State the preparation type.
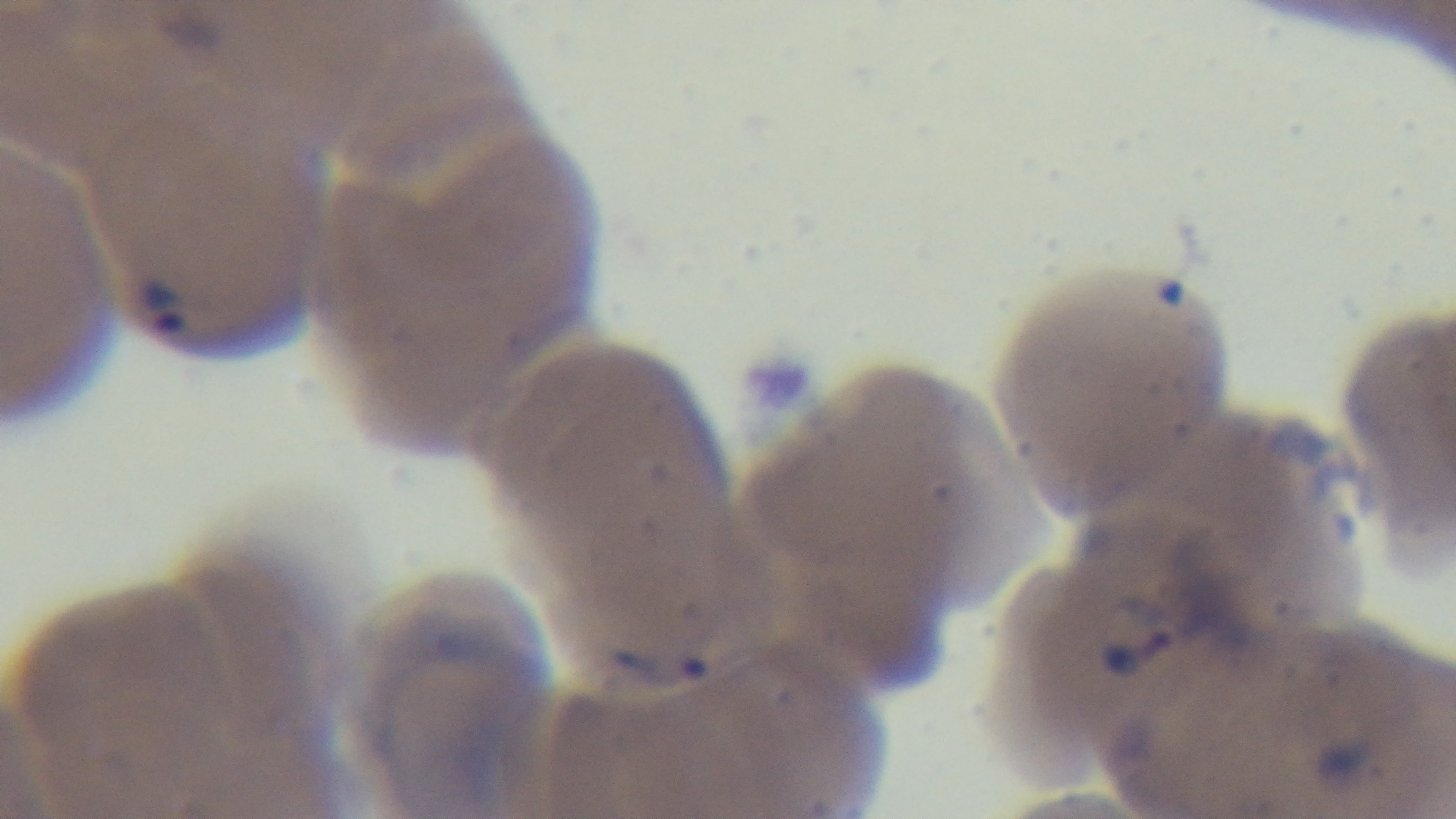
It is a thin blood film.

Summary:
  - Capture: mounted 4K digital camera
  - Objective: 100x oil immersion
  - Stain: Giemsa
  - Field of view: single
  - Modality: light microscopy
  - Malaria status: positive